Name the blood parasite species.
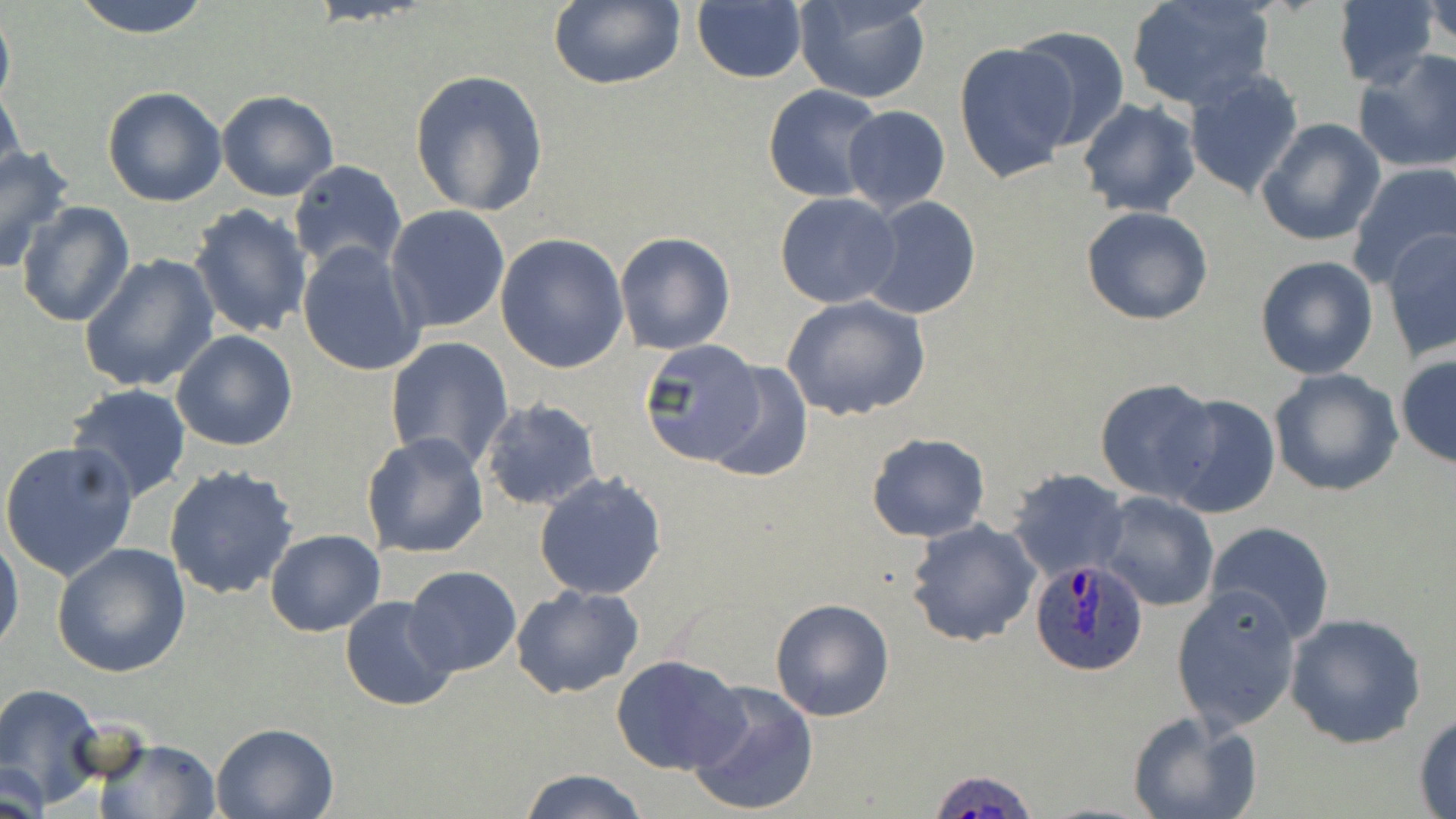
Plasmodium ovale.

Approximate bounding boxes as [x1, y1, x2, y2] in pixels. Uninfected red blood cell locations: [68, 0, 214, 37], [792, 0, 931, 104], [1332, 0, 1444, 89], [1124, 1, 1275, 110], [545, 2, 686, 91], [1426, 2, 1456, 52], [691, 3, 808, 84], [0, 7, 14, 118], [1013, 27, 1131, 149], [953, 42, 1079, 184], [1354, 51, 1456, 174], [409, 69, 550, 216], [1183, 70, 1304, 199], [0, 85, 25, 194], [763, 85, 888, 201], [103, 86, 229, 207], [216, 90, 339, 202], [1077, 98, 1202, 219], [842, 105, 950, 213], [1255, 119, 1385, 246], [0, 143, 75, 272], [289, 161, 407, 276], [1348, 161, 1456, 287], [775, 192, 902, 308], [860, 197, 982, 320], [17, 199, 135, 327], [187, 204, 313, 341], [386, 204, 510, 333], [1081, 205, 1214, 325], [1382, 229, 1456, 361], [615, 232, 737, 355], [495, 233, 628, 374], [295, 241, 425, 378], [78, 253, 221, 395], [1255, 256, 1379, 378], [781, 295, 932, 422], [172, 330, 298, 452], [384, 336, 514, 472], [639, 339, 772, 473], [1395, 354, 1456, 468], [700, 361, 812, 486], [1269, 368, 1403, 497], [1095, 379, 1220, 502], [64, 384, 192, 504], [1160, 393, 1283, 518], [480, 398, 603, 511], [866, 432, 989, 542], [361, 433, 490, 558], [0, 441, 139, 582], [164, 463, 299, 599], [1007, 469, 1129, 581], [534, 472, 668, 600], [1094, 491, 1220, 612], [905, 518, 1041, 647], [1204, 521, 1335, 646], [0, 530, 23, 657], [264, 530, 384, 638], [52, 542, 191, 678], [403, 565, 521, 677], [1171, 583, 1302, 733], [511, 584, 644, 699], [339, 596, 458, 712], [769, 597, 895, 722], [1285, 611, 1427, 747], [611, 653, 747, 776], [686, 682, 819, 817], [0, 683, 108, 810], [1126, 709, 1261, 819], [1412, 710, 1456, 817], [209, 722, 339, 818], [92, 736, 223, 818], [1, 762, 50, 818], [521, 769, 649, 819]. Plasmodium ovale-infected red blood cell locations: [1028, 558, 1148, 677], [929, 769, 1041, 819]. One field of a larger specimen. Captured at 1000x magnification. Thin blood smear. Image is 1456×819 pixels. Light microscopy. May-Grünwald-Giemsa stain.